State which cell type is depicted.
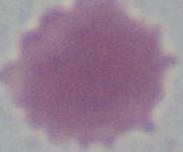

An erythrocyte.

Photomicrograph. 1000x magnification.